Locate every blood parasite and identify its species.
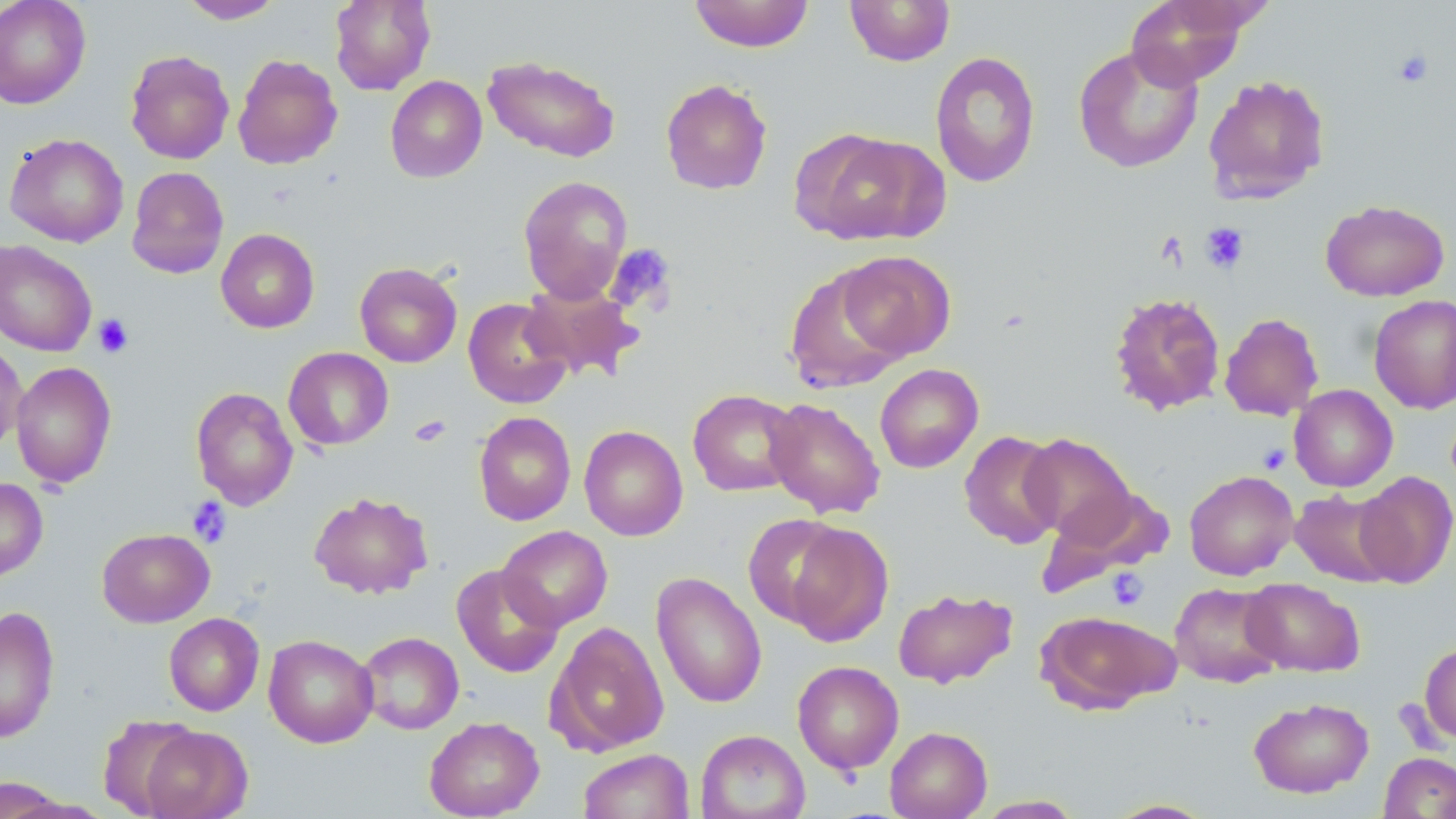
No blood parasites seen.

slide-level diagnosis = negative for blood parasites
image size = 1456×819 pixels
magnification = 1000x
preparation = thin blood smear
uninfected red blood cell locations = approximate bounding boxes as (x1, y1, x2, y2) in pixels: (0, 0, 91, 109), (178, 0, 285, 24), (330, 0, 435, 95), (688, 0, 814, 53), (844, 0, 956, 66), (1124, 0, 1252, 89), (1073, 44, 1204, 173), (125, 50, 234, 164), (929, 50, 1041, 188), (232, 54, 342, 169), (482, 55, 621, 163), (1202, 74, 1331, 203), (385, 75, 487, 182), (660, 78, 773, 195), (795, 128, 947, 247), (4, 133, 128, 247), (126, 166, 229, 279), (518, 175, 633, 304), (1320, 199, 1449, 302), (215, 228, 320, 333), (0, 240, 97, 356), (837, 250, 955, 361), (354, 261, 462, 368), (784, 267, 908, 393), (520, 281, 644, 382), (1109, 291, 1226, 415), (1368, 294, 1456, 414), (463, 298, 572, 409), (1219, 313, 1323, 421), (0, 337, 27, 455), (283, 347, 394, 450), (10, 360, 117, 489), (874, 363, 984, 473), (1289, 385, 1398, 491), (190, 387, 299, 510), (687, 389, 802, 496), (763, 397, 886, 518), (474, 411, 576, 526), (579, 424, 688, 541), (959, 430, 1065, 548), (1019, 432, 1137, 544), (1184, 470, 1299, 580), (1354, 471, 1456, 588), (0, 477, 48, 581), (1038, 485, 1171, 594), (1288, 489, 1400, 588), (308, 490, 433, 599), (743, 513, 851, 626), (783, 521, 894, 647), (497, 525, 612, 631), (97, 528, 215, 627), (451, 564, 565, 678), (651, 572, 768, 708), (1241, 577, 1365, 677), (1169, 582, 1284, 687), (892, 587, 1018, 689), (0, 606, 60, 743), (1036, 610, 1178, 714), (164, 613, 264, 716), (545, 621, 669, 757), (357, 631, 463, 735), (263, 634, 378, 748), (1419, 641, 1456, 744), (792, 661, 904, 774), (1248, 697, 1374, 798), (97, 714, 201, 817), (424, 716, 544, 818), (139, 724, 252, 818), (885, 726, 993, 819), (695, 729, 811, 819), (578, 749, 694, 819), (1378, 752, 1456, 818), (0, 777, 70, 818), (973, 795, 1086, 818), (1104, 798, 1219, 818)
platelet locations = approximate bounding boxes as (x1, y1, x2, y2) in pixels: (1392, 48, 1434, 88), (1200, 222, 1249, 273), (605, 243, 677, 314), (94, 314, 133, 358), (411, 415, 452, 447), (1257, 444, 1292, 474), (187, 496, 232, 548), (1106, 567, 1149, 611)
field of view = one of a larger specimen
modality = light microscopy
stain = May-Grünwald-Giemsa